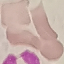 Malaria status: uninfected. Giemsa-stained preparation. Cell patch, automatically extracted from a larger field of view and resized to 64 × 64 pixels. Thin smear of blood. Acquired by smartphone through the microscope eyepiece.